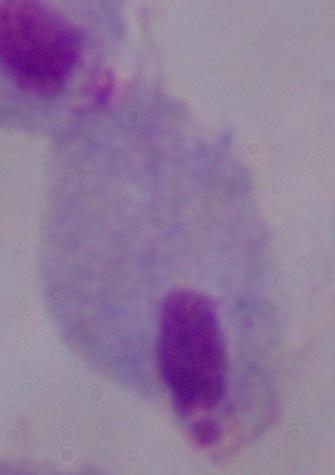
modality = photomicrograph
identification = trichomonad
magnification = 1000x